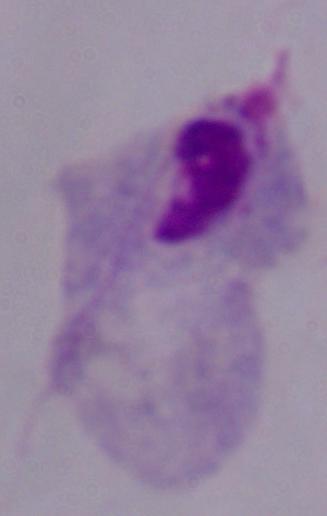

A trichomonad is seen. 1000x magnification. Micrograph.